Outline each Plasmodium falciparum-infected red blood cell.
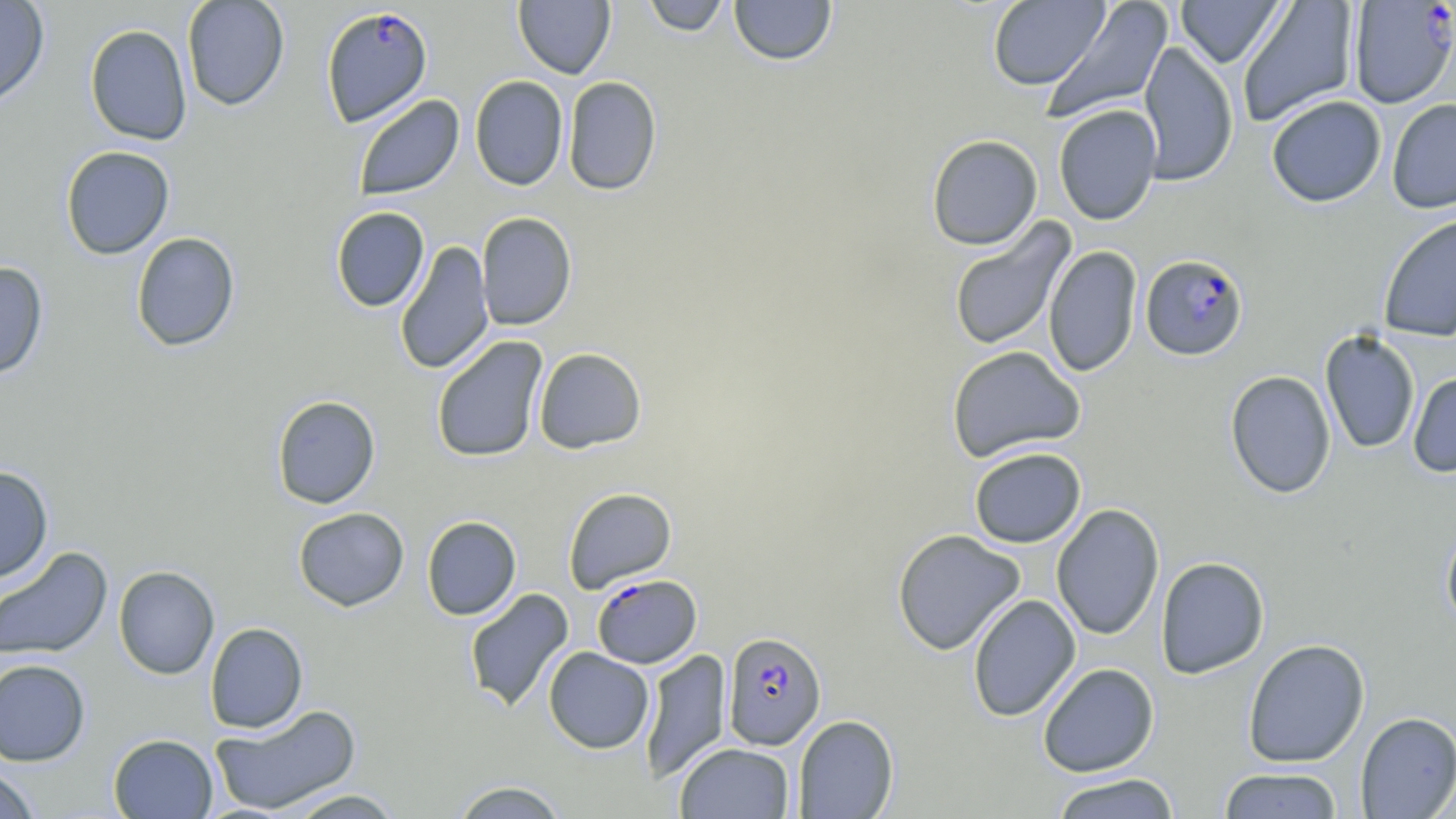
Approximate bounding boxes as [x1, y1, x2, y2] in pixels.
Plasmodium falciparum-infected red blood cells: [1349, 2, 1456, 108], [321, 6, 434, 129], [1140, 254, 1249, 361], [592, 572, 702, 668], [722, 631, 826, 750].

Summary:
  - Uninfected red blood cell locations: [0, 0, 50, 109], [181, 0, 290, 111], [513, 0, 616, 79], [639, 0, 732, 36], [728, 0, 837, 66], [1175, 0, 1287, 68], [1236, 0, 1359, 127], [988, 1, 1110, 90], [1042, 1, 1173, 124], [84, 24, 192, 145], [1137, 41, 1238, 187], [469, 75, 569, 191], [562, 76, 662, 196], [353, 94, 465, 200], [1266, 95, 1387, 207], [1386, 98, 1456, 214], [1053, 104, 1162, 225], [926, 134, 1043, 250], [60, 145, 175, 260], [330, 206, 430, 312], [476, 212, 577, 331], [1378, 212, 1456, 342], [948, 220, 1075, 352], [131, 232, 240, 352], [394, 240, 494, 375], [1043, 245, 1142, 378], [0, 260, 50, 380], [1319, 330, 1421, 454], [431, 335, 548, 463], [946, 345, 1086, 463], [533, 347, 647, 454], [1224, 370, 1336, 499], [1408, 371, 1456, 479], [271, 395, 380, 509], [968, 447, 1086, 548], [0, 465, 54, 584], [563, 487, 677, 593], [1051, 503, 1165, 640], [293, 507, 409, 611], [422, 516, 521, 620], [1440, 523, 1456, 634], [892, 528, 1026, 656], [0, 546, 113, 662], [1155, 556, 1270, 679], [113, 565, 220, 680], [463, 588, 575, 713], [967, 594, 1081, 722], [205, 622, 308, 733], [1243, 638, 1370, 768], [544, 647, 654, 754], [639, 648, 731, 783], [0, 658, 91, 766], [1037, 662, 1160, 777], [209, 704, 362, 816], [1355, 711, 1456, 818], [792, 714, 899, 818], [108, 733, 218, 818], [674, 742, 795, 819], [0, 765, 41, 819], [1218, 767, 1344, 818], [1049, 772, 1181, 818], [450, 780, 570, 819], [282, 789, 405, 818]
  - Slide-level diagnosis: Plasmodium falciparum
  - Field of view: single
  - Preparation: thin blood smear
  - Modality: light microscopy
  - Magnification: 1000x
  - Image size: 1456×819 pixels
  - Stain: May-Grünwald-Giemsa